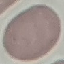
Summary:
  - Result: negative for malaria parasites
  - Stain: Giemsa
  - Preparation: thin blood smear
  - Capture: smartphone camera at the microscope eyepiece
  - Image type: cell patch, automatically extracted from a larger field of view and resized to 64 × 64 pixels